Classify this cell by malaria status.
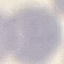

Uninfected.

image type = automatically extracted cell patch, resized to 64 × 64 pixels
stain = Giemsa
capture = smartphone through the microscope eyepiece
preparation = thin blood film